Outline each blood parasite and name the species.
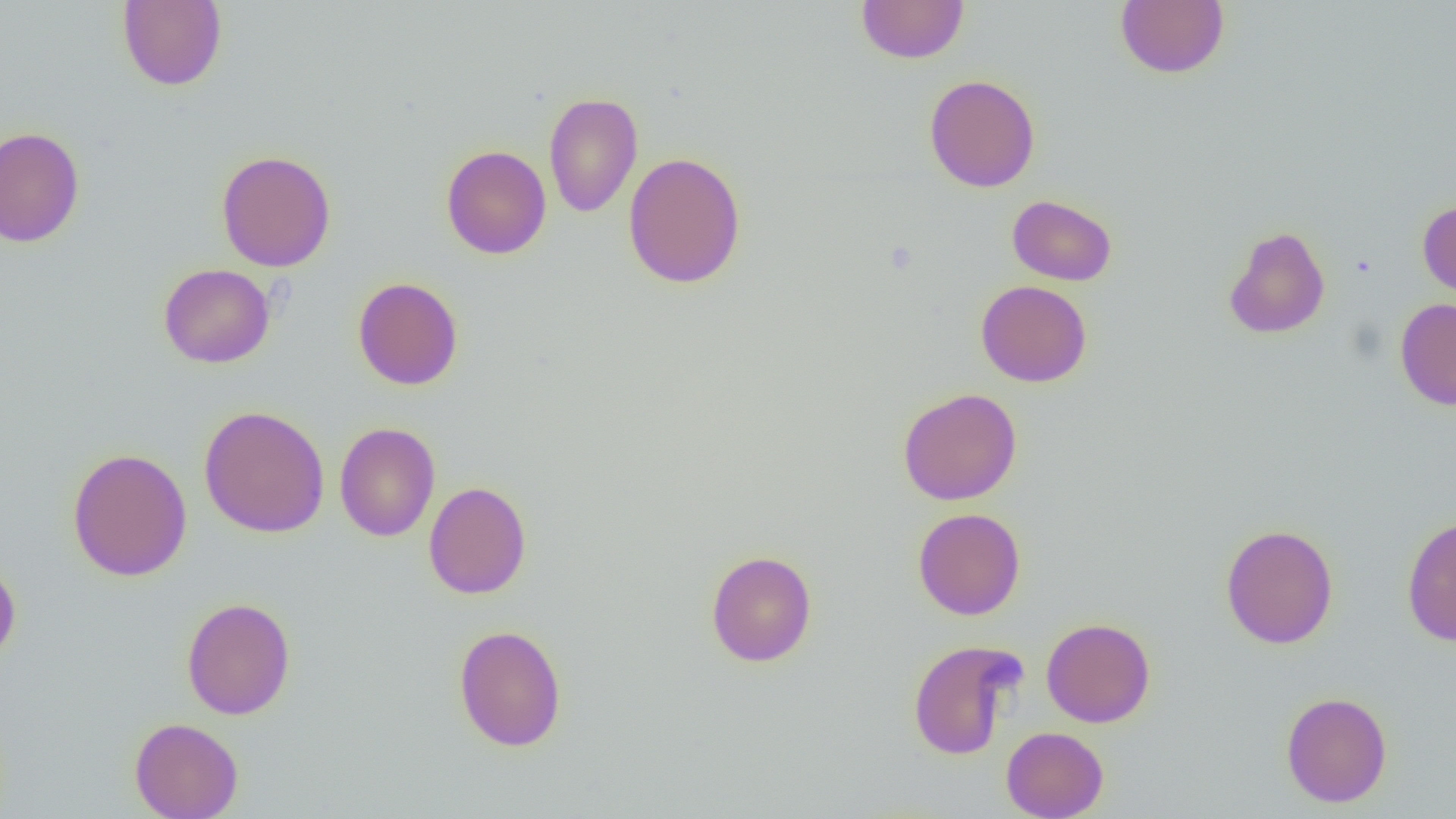

No blood parasites seen.

slide-level diagnosis = negative for blood parasites
field of view = single
image size = 1456×819 pixels
magnification = 1000x
uninfected red blood cell locations = approximate bounding boxes as (x1, y1, x2, y2) in pixels: (117, 0, 227, 91), (1115, 0, 1229, 79), (856, 1, 970, 64), (924, 74, 1040, 192), (543, 92, 643, 218), (0, 126, 85, 248), (441, 145, 552, 259), (216, 150, 336, 271), (622, 151, 746, 289), (1007, 194, 1117, 286), (1417, 200, 1456, 301), (1223, 225, 1331, 339), (158, 263, 275, 368), (353, 277, 463, 390), (975, 280, 1092, 387), (1394, 298, 1456, 410), (897, 387, 1022, 505), (198, 405, 330, 538), (334, 422, 440, 542), (67, 447, 192, 581), (423, 481, 531, 600), (912, 507, 1026, 620), (1401, 514, 1456, 647), (1220, 523, 1339, 650), (705, 550, 817, 667), (0, 561, 21, 669), (181, 597, 295, 720), (1041, 618, 1156, 727), (453, 624, 567, 751), (907, 639, 1025, 760), (1280, 691, 1393, 808), (129, 717, 244, 819), (1001, 726, 1109, 819)
preparation = thin blood film
modality = optical microscopy